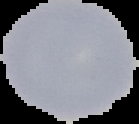
image_size: 139×124 pixels
preparation: thin blood smear
malaria_status: uninfected
image_type: segmented cell region on a black background